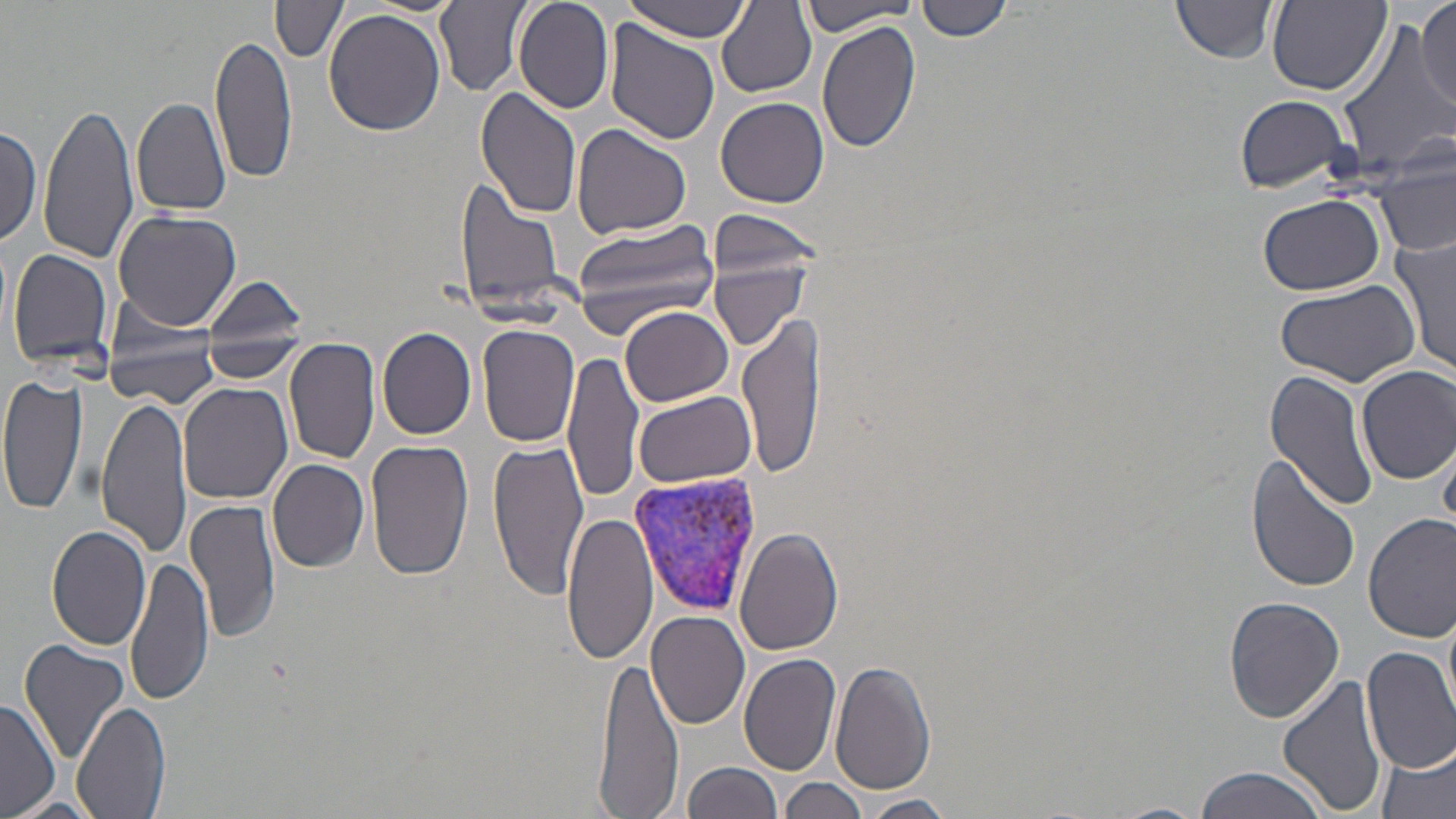
Plasmodium vivax-infected red blood cell locations = approximate bounding boxes as named x1/y1/x2/y2 corners in pixels: (x1=628, y1=471, x2=765, y2=617)
slide-level diagnosis = Plasmodium vivax
modality = optical microscopy
uninfected red blood cell locations = approximate bounding boxes as named x1/y1/x2/y2 corners in pixels: (x1=360, y1=0, x2=467, y2=15), (x1=435, y1=0, x2=531, y2=94), (x1=513, y1=0, x2=614, y2=114), (x1=917, y1=0, x2=1013, y2=42), (x1=1171, y1=0, x2=1280, y2=63), (x1=616, y1=1, x2=756, y2=41), (x1=1268, y1=1, x2=1392, y2=95), (x1=1416, y1=1, x2=1456, y2=109), (x1=273, y1=2, x2=349, y2=62), (x1=715, y1=2, x2=816, y2=99), (x1=800, y1=2, x2=920, y2=35), (x1=325, y1=8, x2=447, y2=137), (x1=816, y1=18, x2=919, y2=154), (x1=1336, y1=19, x2=1455, y2=179), (x1=606, y1=22, x2=721, y2=147), (x1=208, y1=31, x2=295, y2=188), (x1=475, y1=87, x2=583, y2=221), (x1=1234, y1=94, x2=1355, y2=193), (x1=130, y1=95, x2=230, y2=219), (x1=715, y1=95, x2=829, y2=206), (x1=38, y1=99, x2=137, y2=267), (x1=0, y1=120, x2=43, y2=250), (x1=572, y1=125, x2=691, y2=239), (x1=1378, y1=149, x2=1456, y2=263), (x1=456, y1=178, x2=568, y2=316), (x1=1256, y1=192, x2=1387, y2=296), (x1=113, y1=209, x2=240, y2=333), (x1=709, y1=211, x2=825, y2=279), (x1=568, y1=216, x2=726, y2=331), (x1=1393, y1=236, x2=1455, y2=376), (x1=8, y1=247, x2=117, y2=374), (x1=706, y1=249, x2=815, y2=352), (x1=201, y1=275, x2=311, y2=372), (x1=1274, y1=277, x2=1421, y2=388), (x1=620, y1=306, x2=733, y2=407), (x1=738, y1=312, x2=825, y2=479), (x1=478, y1=324, x2=583, y2=446), (x1=377, y1=328, x2=477, y2=439), (x1=285, y1=338, x2=381, y2=467), (x1=104, y1=344, x2=222, y2=405), (x1=562, y1=352, x2=642, y2=504), (x1=1356, y1=365, x2=1456, y2=483), (x1=1264, y1=370, x2=1379, y2=512), (x1=0, y1=372, x2=87, y2=520), (x1=178, y1=382, x2=293, y2=503), (x1=632, y1=391, x2=758, y2=489), (x1=94, y1=393, x2=190, y2=559), (x1=488, y1=438, x2=590, y2=598), (x1=367, y1=439, x2=475, y2=583), (x1=1247, y1=456, x2=1361, y2=594), (x1=266, y1=457, x2=370, y2=573), (x1=187, y1=497, x2=282, y2=643), (x1=561, y1=508, x2=658, y2=667), (x1=1364, y1=513, x2=1456, y2=642), (x1=46, y1=522, x2=153, y2=650), (x1=735, y1=527, x2=843, y2=657), (x1=126, y1=556, x2=214, y2=707), (x1=1224, y1=596, x2=1344, y2=721), (x1=647, y1=611, x2=750, y2=729), (x1=17, y1=637, x2=129, y2=761), (x1=1361, y1=646, x2=1456, y2=772), (x1=738, y1=651, x2=842, y2=776), (x1=596, y1=658, x2=682, y2=815), (x1=830, y1=658, x2=937, y2=795), (x1=1277, y1=675, x2=1390, y2=816), (x1=0, y1=701, x2=61, y2=818), (x1=73, y1=701, x2=171, y2=819), (x1=1377, y1=742, x2=1455, y2=819), (x1=682, y1=761, x2=785, y2=819), (x1=1192, y1=765, x2=1334, y2=819), (x1=780, y1=778, x2=871, y2=819), (x1=858, y1=794, x2=956, y2=818), (x1=6, y1=796, x2=104, y2=819), (x1=1109, y1=802, x2=1211, y2=819)
image size = 1456×819 pixels
stain = May-Grünwald-Giemsa
magnification = 1000x
preparation = thin blood smear
field of view = one of a larger specimen